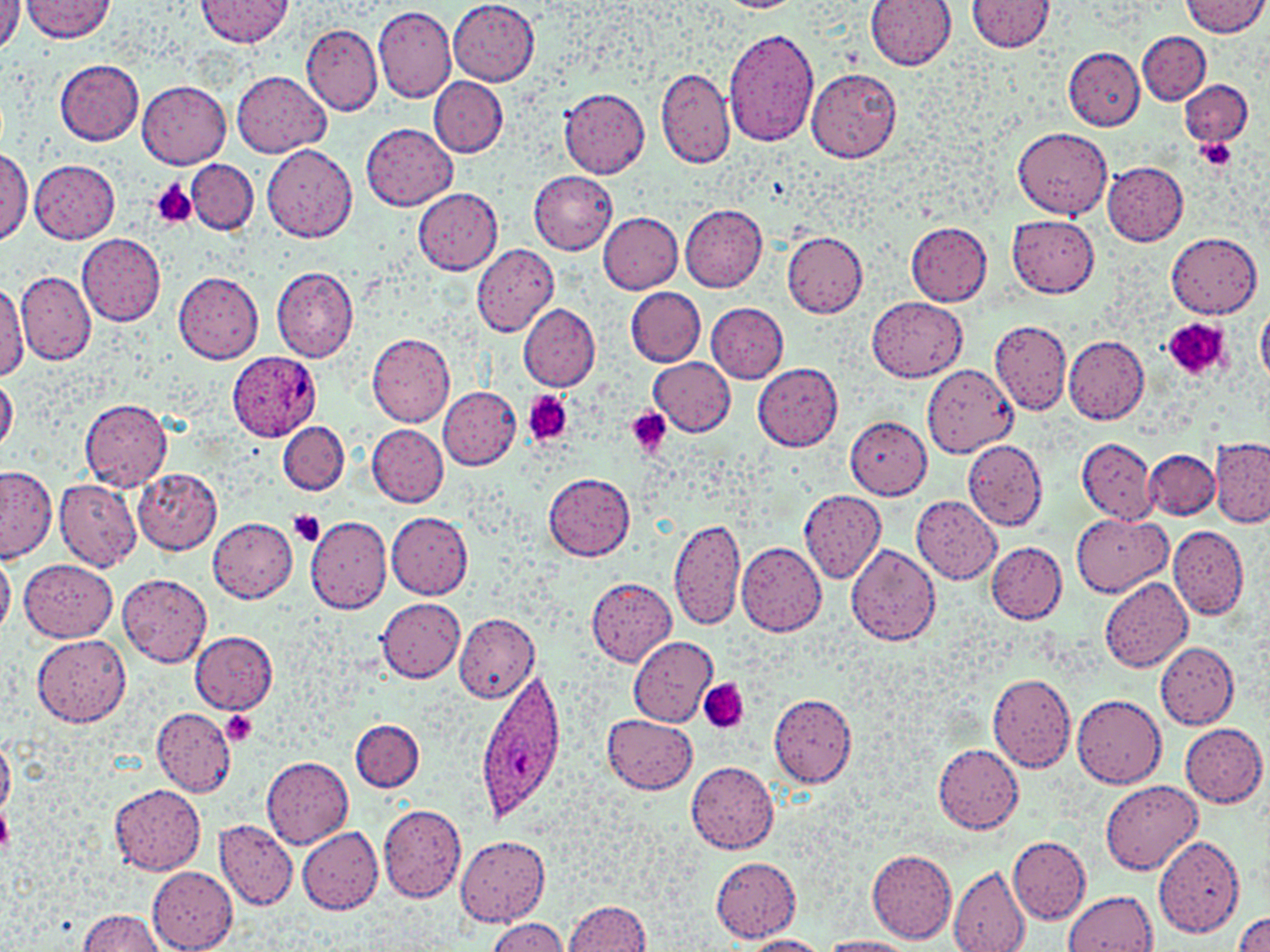

{
  "plasmodium_ovale_infected_red_blood_cell_locations": "approximate bounding boxes as (x1, y1, x2, y2) in pixels: (227, 352, 321, 440), (473, 669, 568, 822)",
  "slide_level_diagnosis": "Plasmodium ovale",
  "platelet_locations": "approximate bounding boxes as (x1, y1, x2, y2) in pixels: (1196, 137, 1238, 172), (148, 180, 197, 229), (1162, 318, 1231, 379), (523, 391, 573, 446), (626, 407, 672, 458), (287, 509, 327, 547), (698, 680, 748, 735), (219, 712, 259, 746), (0, 805, 12, 856)",
  "modality": "optical microscopy",
  "field_of_view": "single",
  "uninfected_red_blood_cell_locations": "approximate bounding boxes as (x1, y1, x2, y2) in pixels: (21, 0, 117, 42), (196, 0, 294, 47), (866, 0, 956, 69), (1183, 0, 1266, 35), (0, 1, 23, 52), (448, 1, 540, 85), (965, 1, 1055, 53), (373, 6, 457, 103), (302, 24, 383, 116), (723, 27, 819, 145), (1137, 31, 1210, 105), (1063, 47, 1145, 130), (55, 59, 145, 144), (655, 68, 734, 169), (807, 69, 900, 164), (233, 71, 330, 157), (430, 77, 509, 156), (137, 78, 232, 167), (1181, 79, 1252, 147), (558, 88, 651, 178), (362, 123, 457, 210), (1013, 127, 1112, 218), (263, 144, 357, 243), (0, 148, 31, 247), (30, 158, 120, 243), (187, 159, 258, 234), (1102, 160, 1189, 245), (529, 171, 617, 255), (412, 187, 503, 274), (679, 205, 768, 292), (597, 211, 683, 292), (1007, 216, 1100, 297), (905, 221, 993, 306), (782, 230, 867, 316), (1167, 232, 1262, 318), (76, 234, 167, 325), (471, 244, 559, 338), (271, 267, 359, 362), (16, 270, 97, 365), (173, 272, 264, 362), (0, 282, 29, 377), (625, 287, 707, 367), (868, 296, 967, 381), (519, 303, 601, 390), (706, 303, 788, 383), (1258, 306, 1270, 384), (989, 319, 1071, 416), (367, 334, 456, 426), (1063, 334, 1150, 422), (649, 357, 735, 436), (753, 363, 844, 451), (924, 366, 1017, 454), (1, 377, 18, 453), (439, 387, 521, 469), (80, 399, 173, 491), (844, 415, 932, 498), (278, 420, 349, 494), (368, 425, 448, 508), (1077, 438, 1158, 525), (1210, 439, 1270, 527), (962, 443, 1047, 540), (1143, 449, 1218, 520), (1, 467, 56, 561), (133, 468, 222, 554), (544, 472, 636, 560), (55, 480, 141, 572), (798, 490, 886, 582), (911, 495, 1002, 584), (1072, 512, 1170, 596), (386, 513, 472, 599), (304, 516, 391, 614), (207, 517, 298, 603), (670, 518, 746, 631), (1169, 525, 1249, 620), (987, 541, 1066, 623), (736, 542, 827, 637), (846, 544, 941, 645), (0, 547, 15, 636), (20, 558, 118, 640), (118, 574, 212, 668), (1100, 577, 1193, 672), (586, 579, 675, 666), (377, 598, 465, 682), (453, 614, 541, 701), (189, 630, 277, 713), (33, 635, 129, 727), (629, 636, 719, 727), (1155, 643, 1239, 729), (987, 673, 1076, 771), (770, 693, 857, 786), (1072, 693, 1167, 788), (152, 708, 236, 796), (603, 714, 697, 794), (351, 719, 424, 792), (1181, 724, 1267, 806), (0, 735, 15, 817), (933, 744, 1023, 833), (263, 757, 353, 847), (686, 761, 779, 853), (1101, 780, 1203, 873), (110, 785, 206, 876), (379, 802, 467, 902), (214, 821, 297, 911), (297, 824, 383, 915), (1151, 835, 1244, 938), (455, 837, 550, 926), (1009, 837, 1091, 923), (867, 849, 958, 942), (711, 857, 801, 941), (148, 867, 237, 952), (948, 868, 1031, 952), (1066, 892, 1157, 952), (563, 900, 653, 952), (77, 909, 166, 951), (1231, 910, 1270, 952), (487, 918, 567, 952), (740, 936, 829, 952), (817, 937, 916, 952)",
  "preparation": "thin blood smear",
  "image_size": "1270×952 pixels",
  "magnification": "1000x",
  "stain": "May-Grünwald-Giemsa"
}